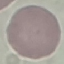

Result: no malaria parasites detected. Thin blood smear. Giemsa-stained preparation. Acquired by smartphone through the microscope eyepiece. Cell patch, automatically extracted from a larger field of view and resized to 64 × 64 pixels.